Name the parasite shown.
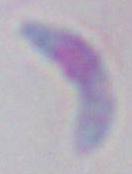
This is Toxoplasma gondii.

modality = photomicrograph
magnification = 1000x